Evaluate for Plasmodium parasites.
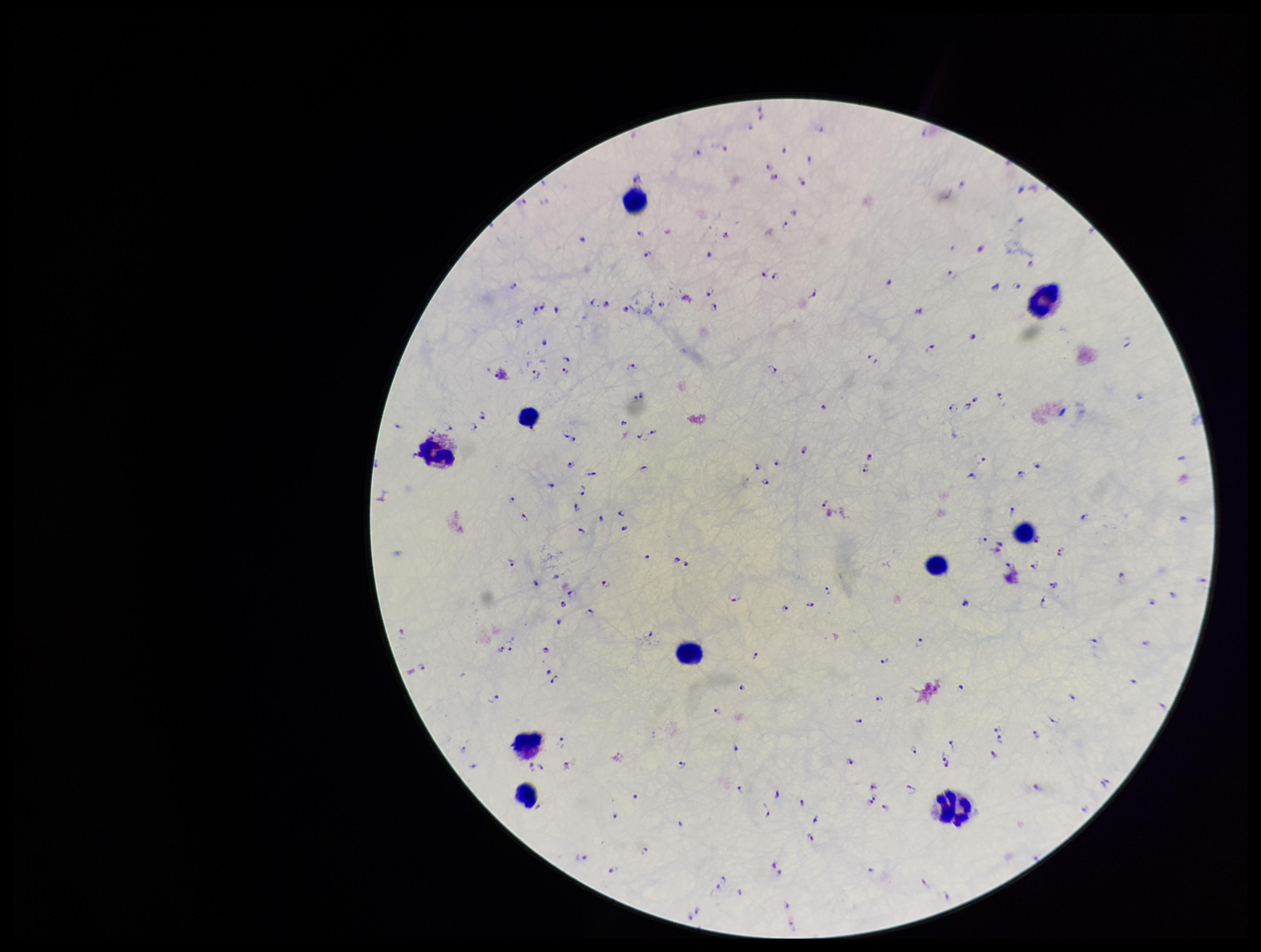
Detected.

Summary:
  - Leukocyte count: 10
  - Preparation: thick
  - Parasite count: 194
  - Stain: Giemsa
  - Image size: 1261×952 pixels
  - Species reported for this patient: Plasmodium falciparum
  - Field of view: one from this slide
  - Capture: smartphone photograph through the microscope eyepiece
  - Patient malaria status: infected